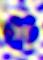

identification: leukocyte
magnification: 400x
modality: photomicrograph